Assess the morphology of the erythrocytes.
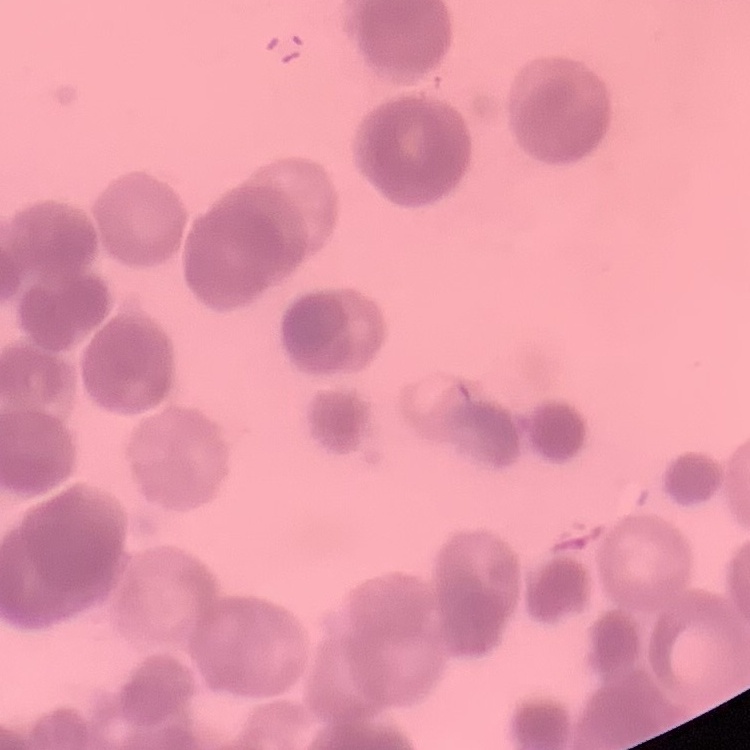
They show rouleaux formation.

image_type: one tile cut from a larger photomicrograph
stain: Field's or Giemsa
preparation: thin peripheral smear